Report the malaria status of this cell.
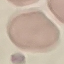

It is uninfected.

preparation = thin blood smear
stain = Giemsa
capture = smartphone through the microscope eyepiece
image type = automatically extracted cell patch, resized to 64 × 64 pixels